Assess this cell for malaria.
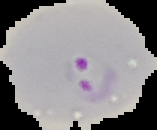
Parasitized.

From a thin blood film. Segmented cell region on a black background. Image is 157×130 pixels.